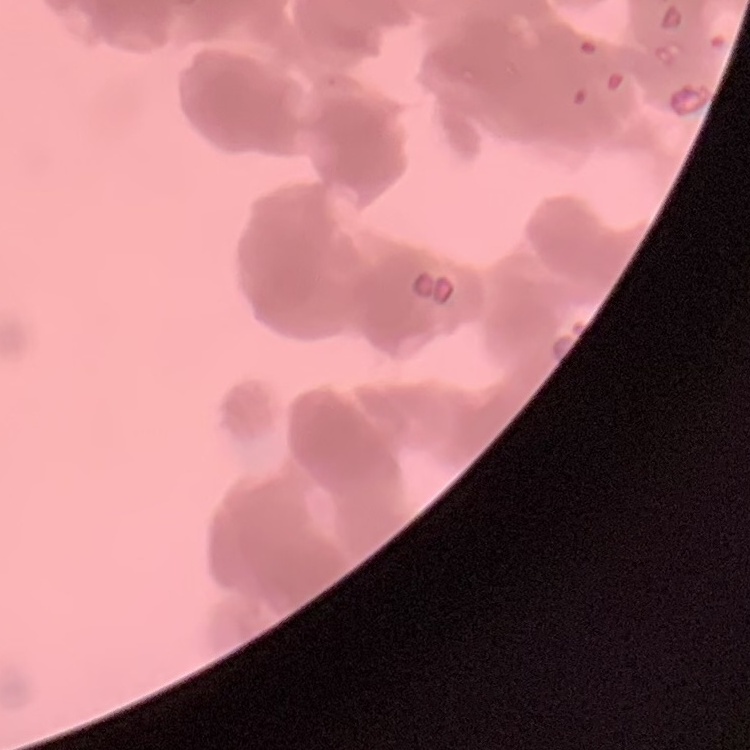

red_blood_cell_morphology: rouleaux formation
image_type: one tile cut from a larger photomicrograph
preparation: thin blood smear
stain: Field's or Giemsa